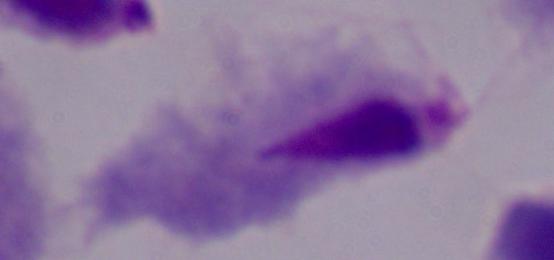

Summary:
  - Magnification: 1000x
  - Modality: photomicrograph
  - Identification: trichomonad